Classify this cell by malaria status.
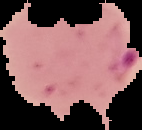

It is parasitized.

preparation = thin blood smear
image size = 142×130 pixels
image type = segmented cell region with the area outside set to black